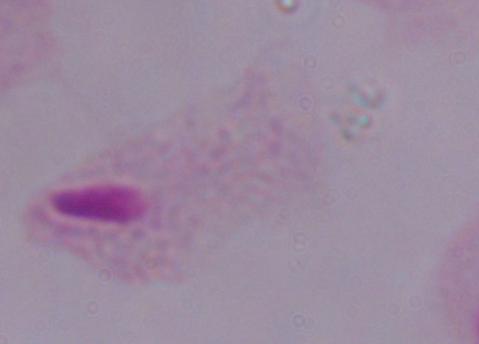
modality = photomicrograph
identification = trichomonad
magnification = 1000x